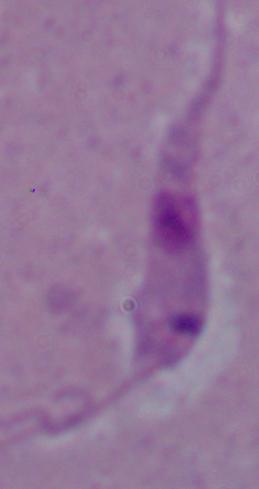

identification = Leishmania
magnification = 1000x
modality = micrograph